Locate every blood parasite and identify its species.
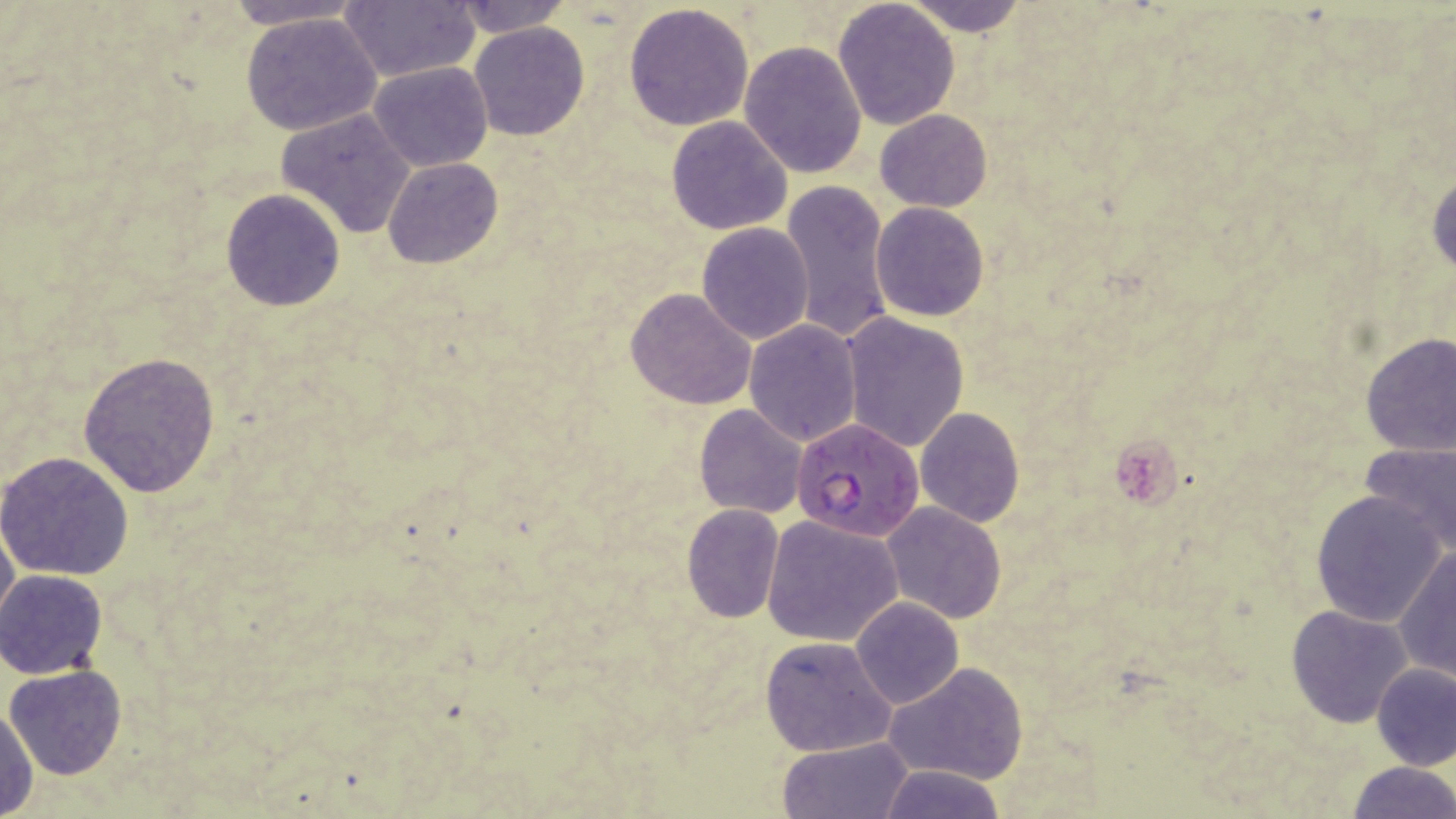

Approximate bounding boxes as (x1, y1, x2, y2) in pixels.
Plasmodium falciparum-infected red blood cells: (792, 417, 925, 540).
No Plasmodium ovale, Plasmodium malariae, Plasmodium vivax, Babesia divergens, or Trypanosoma brucei observed.

Uninfected red blood cell locations: (221, 0, 368, 30), (341, 0, 482, 83), (450, 0, 572, 36), (904, 0, 1029, 37), (833, 1, 961, 130), (624, 2, 754, 132), (242, 12, 384, 137), (468, 22, 589, 140), (740, 41, 869, 178), (368, 62, 492, 171), (276, 108, 418, 236), (875, 110, 993, 211), (666, 116, 792, 236), (384, 158, 502, 269), (1428, 169, 1456, 277), (780, 182, 892, 343), (221, 189, 346, 311), (870, 203, 989, 322), (697, 222, 814, 345), (625, 288, 757, 410), (838, 312, 969, 453), (744, 320, 863, 446), (1358, 332, 1456, 458), (78, 351, 222, 497), (692, 404, 808, 518), (915, 407, 1024, 528), (1359, 441, 1456, 557), (1, 450, 134, 580), (1309, 490, 1445, 627), (881, 502, 1004, 624), (682, 504, 784, 622), (0, 513, 18, 630), (762, 514, 904, 647), (1393, 546, 1456, 681), (0, 569, 108, 679), (850, 597, 962, 708), (1286, 604, 1412, 727), (760, 635, 897, 757), (1370, 661, 1456, 771), (883, 662, 1028, 785), (5, 665, 127, 780), (0, 703, 38, 819), (777, 737, 914, 819), (1345, 760, 1455, 818), (874, 764, 1007, 818). Slide-level diagnosis: Plasmodium falciparum. Light microscopy. One field of a larger specimen. Thin blood smear. Image is 1456×819 pixels. 1000x magnification. May-Grünwald-Giemsa stain.